Locate every Plasmodium parasite.
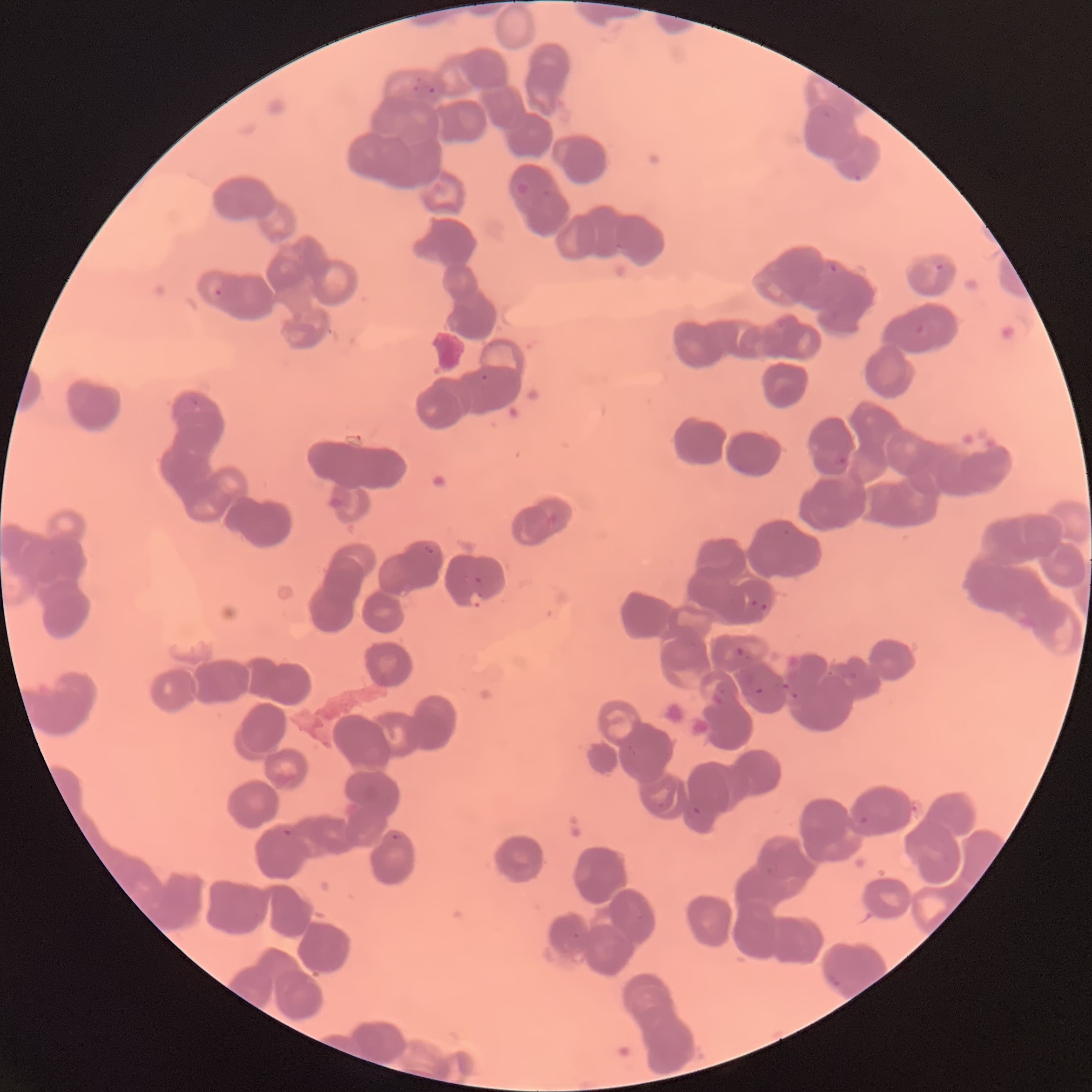
Approximate bounding boxes as (x1, y1, x2, y2) in pixels.
Plasmodium parasites: (413, 76, 422, 92), (422, 84, 435, 97), (821, 111, 832, 119), (852, 174, 864, 182), (515, 181, 531, 195), (541, 188, 552, 199), (611, 242, 626, 252), (826, 262, 838, 273), (935, 262, 945, 273), (214, 289, 223, 299), (912, 322, 926, 335), (479, 374, 488, 390), (185, 397, 199, 408), (833, 450, 850, 468), (542, 513, 558, 528), (782, 529, 791, 537), (421, 543, 436, 557), (471, 576, 483, 587), (470, 590, 483, 608), (751, 598, 769, 612), (624, 745, 635, 757), (651, 797, 665, 811), (686, 804, 701, 818), (854, 816, 872, 827), (280, 825, 293, 837), (391, 833, 403, 841), (762, 865, 778, 876), (633, 911, 651, 932), (572, 931, 581, 940), (826, 973, 842, 989).

The red blood cells show rouleaux formation. Image is 1092×1092 pixels. Thin blood film. Light microscopy.